Classify this cell by malaria status.
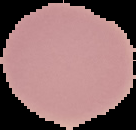

It is uninfected.

From a thin blood smear. Segmented cell region on a black background. Image is 136×130 pixels.